Locate and identify every blood parasite.
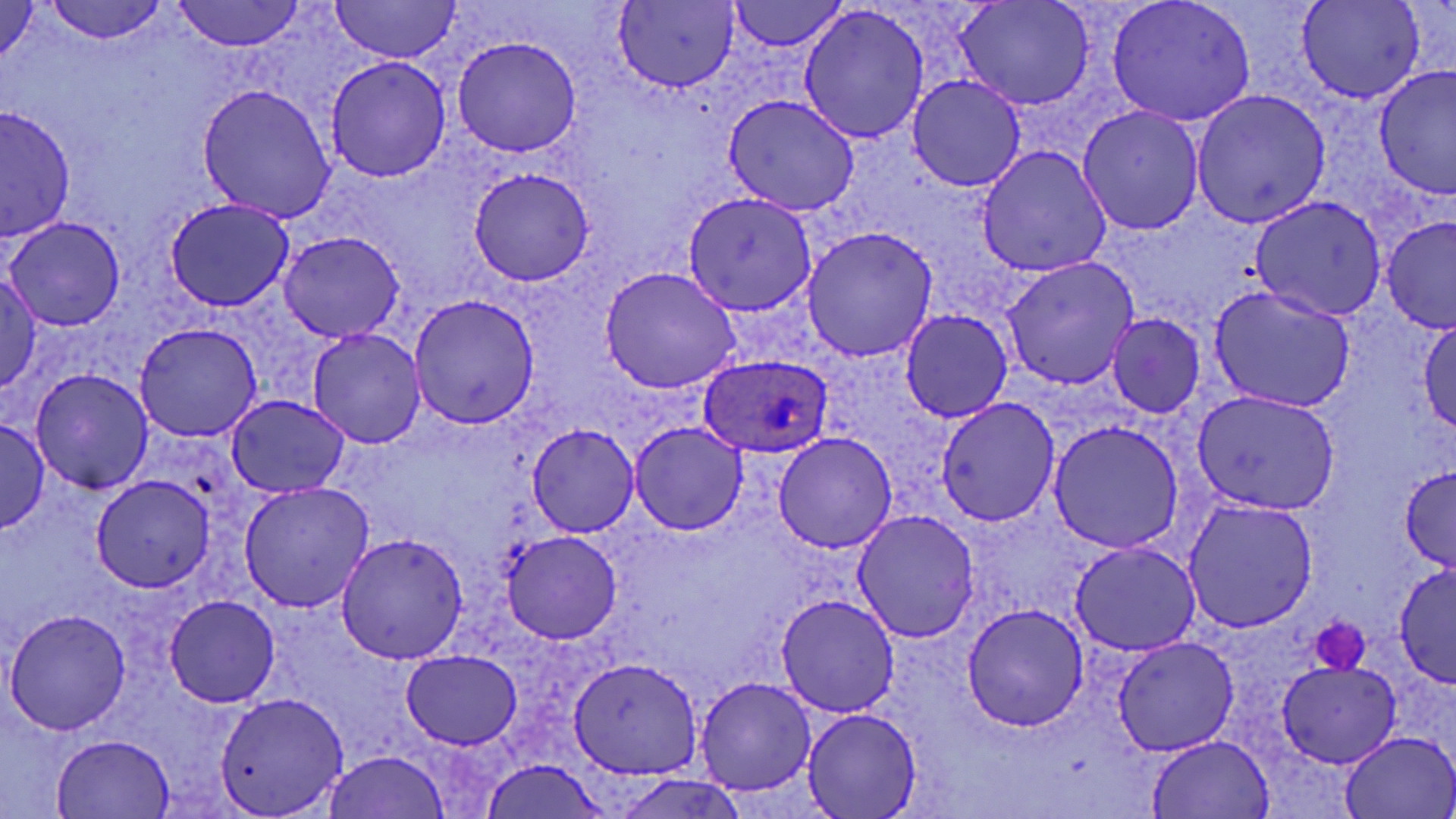
Approximate bounding boxes as [x1, y1, x2, y2] in pixels.
Plasmodium ovale-infected red blood cells: [699, 354, 832, 457].
No Plasmodium falciparum, Plasmodium malariae, Plasmodium vivax, Babesia divergens, or Trypanosoma brucei observed.

slide-level diagnosis = Plasmodium ovale
modality = optical microscopy
preparation = thin blood smear
field of view = single
platelet locations = approximate bounding boxes as [x1, y1, x2, y2] in pixels: [1310, 616, 1370, 673]
uninfected red blood cell locations = approximate bounding boxes as [x1, y1, x2, y2] in pixels: [329, 0, 461, 64], [729, 0, 847, 53], [957, 0, 1095, 110], [1297, 0, 1423, 103], [44, 1, 167, 45], [173, 1, 304, 52], [1106, 1, 1255, 125], [0, 2, 41, 63], [614, 2, 737, 91], [799, 7, 929, 144], [452, 35, 582, 156], [325, 56, 451, 182], [1374, 66, 1455, 198], [908, 73, 1027, 192], [196, 85, 336, 221], [1191, 90, 1331, 229], [722, 97, 859, 216], [1, 106, 76, 244], [1078, 107, 1204, 235], [977, 147, 1111, 276], [469, 168, 594, 286], [683, 191, 816, 315], [1251, 196, 1387, 321], [165, 198, 294, 310], [1381, 216, 1456, 336], [4, 217, 126, 332], [802, 227, 935, 360], [279, 231, 404, 342], [1002, 256, 1139, 389], [600, 267, 741, 394], [0, 275, 44, 392], [1209, 286, 1354, 412], [409, 294, 541, 426], [900, 309, 1013, 424], [1108, 315, 1205, 417], [1417, 318, 1456, 433], [136, 322, 262, 441], [308, 328, 425, 449], [30, 368, 153, 494], [1191, 390, 1340, 516], [227, 396, 348, 497], [935, 397, 1061, 527], [0, 419, 49, 533], [629, 421, 748, 536], [1049, 423, 1184, 552], [526, 424, 640, 536], [772, 433, 897, 553], [1398, 465, 1455, 571], [92, 475, 216, 591], [239, 483, 373, 612], [1182, 499, 1318, 632], [852, 511, 981, 644], [501, 531, 624, 644], [337, 533, 468, 664], [1070, 541, 1201, 655], [1394, 564, 1456, 689], [776, 594, 901, 716], [166, 595, 279, 706], [963, 605, 1087, 731], [7, 609, 130, 733], [1112, 636, 1240, 754], [401, 649, 522, 748], [569, 658, 703, 779], [1276, 659, 1402, 767], [694, 677, 816, 795], [215, 692, 348, 817], [803, 709, 922, 819], [1340, 730, 1456, 818], [52, 734, 176, 818], [1145, 734, 1276, 818], [323, 750, 452, 819], [479, 761, 612, 819], [612, 774, 753, 819]
image size = 1456×819 pixels
magnification = 1000x
stain = May-Grünwald-Giemsa